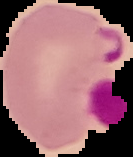
Summary:
  - Image size: 133×157 pixels
  - Result: malaria parasites detected
  - Preparation: thin blood film
  - Image type: segmented cell region on a black background